Classify this cell by malaria status.
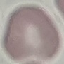
It is uninfected.

capture = smartphone camera at the microscope eyepiece
preparation = thin blood smear
image type = cell patch, automatically extracted from a larger field of view and resized to 64 × 64 pixels
stain = Giemsa